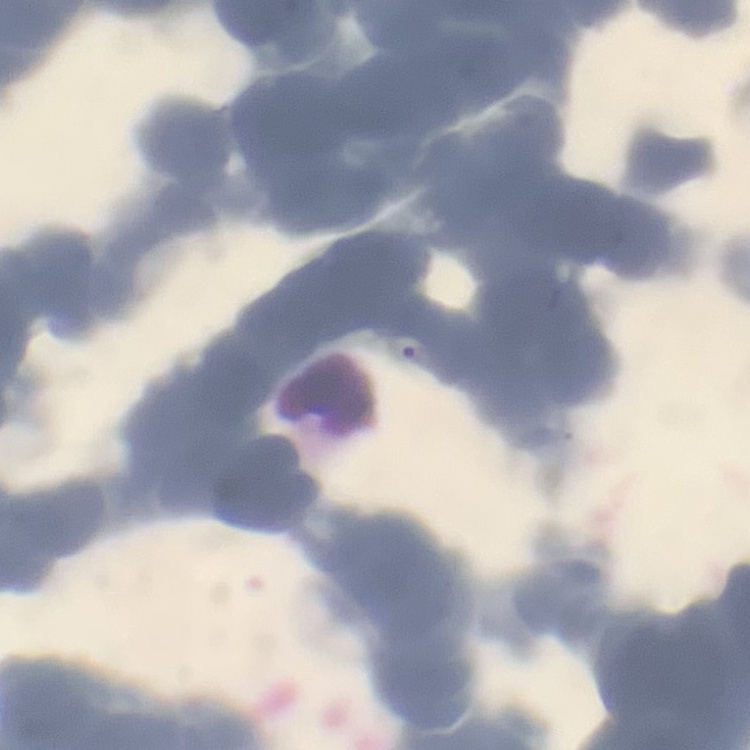

The red blood cells exhibit rouleaux formation. One tile cut from a larger photomicrograph. Thin blood smear. Stained with either Field's or Giemsa.